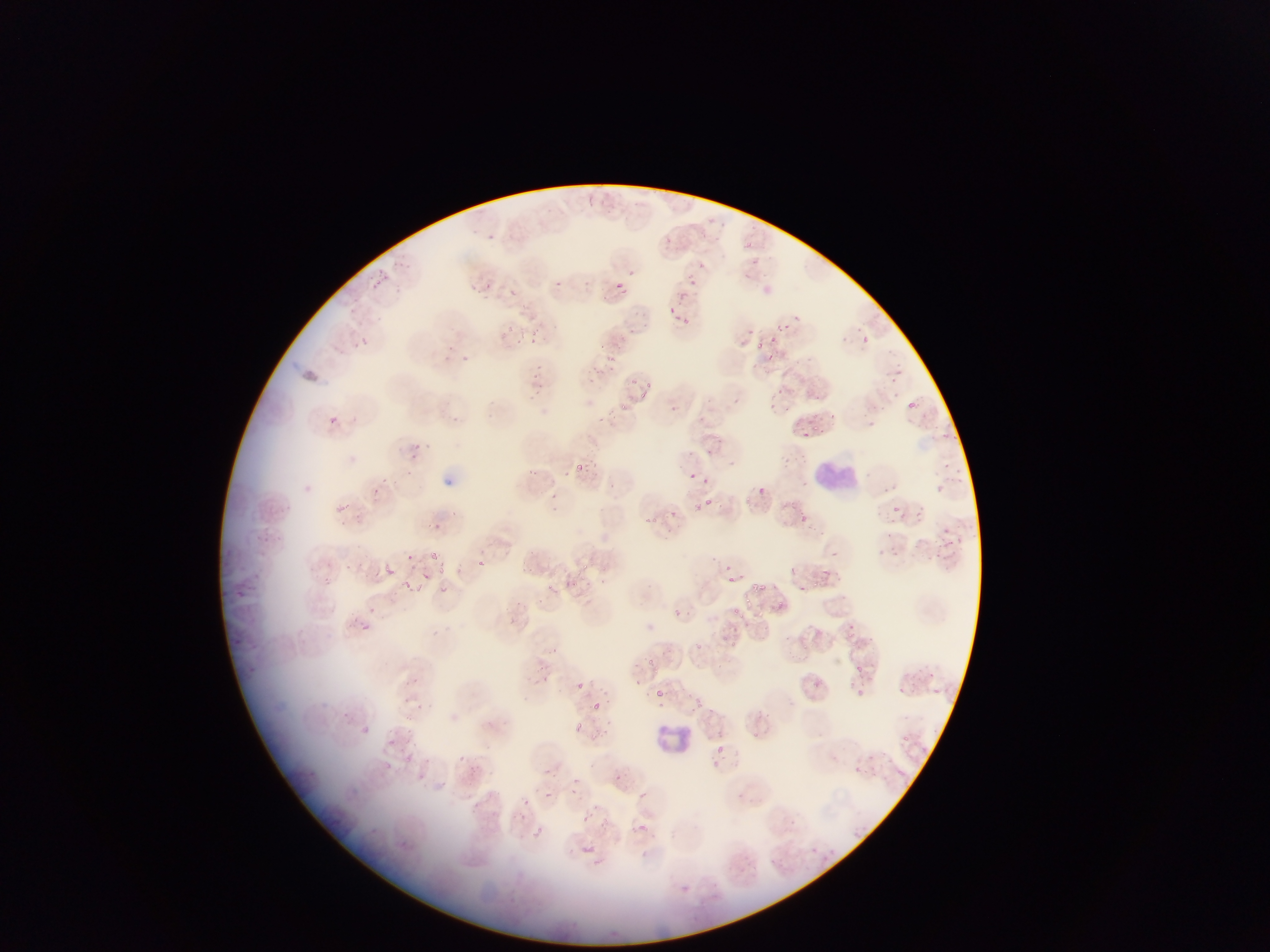

Approximate bounding boxes as [left, top, right, bottom] in pixels. Leukocyte locations: [810, 455, 858, 498], [652, 716, 700, 759]. Plasmodium parasite locations: [471, 230, 485, 239], [488, 233, 499, 244], [714, 234, 721, 244], [665, 235, 674, 248], [746, 241, 754, 248], [698, 261, 709, 274], [628, 268, 634, 276], [371, 273, 388, 287], [685, 275, 698, 287], [556, 280, 566, 288], [612, 280, 628, 296], [467, 283, 481, 292], [483, 283, 496, 294], [508, 288, 519, 297], [678, 290, 690, 301], [669, 306, 674, 314], [682, 315, 690, 324], [777, 315, 799, 334], [502, 318, 524, 346], [642, 322, 648, 331], [849, 322, 872, 348], [532, 327, 541, 337], [521, 329, 527, 339], [357, 334, 371, 348], [767, 335, 775, 344], [755, 339, 762, 350], [444, 342, 454, 349], [460, 354, 470, 363], [605, 354, 614, 362], [593, 366, 603, 372], [585, 371, 597, 381], [532, 372, 540, 379], [630, 379, 640, 384], [645, 379, 657, 388], [637, 387, 651, 400], [533, 388, 544, 397], [906, 392, 924, 411], [617, 401, 627, 410], [668, 404, 679, 413], [607, 407, 618, 416], [328, 414, 340, 426], [599, 416, 615, 425], [797, 421, 811, 446], [812, 424, 818, 432], [410, 442, 420, 451], [574, 463, 587, 474], [690, 471, 701, 482], [758, 484, 767, 496], [744, 494, 753, 503], [705, 498, 713, 504], [891, 505, 901, 513], [798, 512, 809, 523], [646, 514, 658, 523], [406, 548, 423, 565], [428, 551, 438, 560], [478, 559, 487, 568], [581, 562, 592, 572], [381, 566, 400, 579], [438, 568, 448, 578], [424, 573, 437, 583], [728, 575, 736, 584], [580, 577, 589, 581], [573, 580, 584, 589], [811, 581, 818, 589], [400, 582, 410, 591], [546, 582, 559, 594], [753, 583, 767, 591], [797, 584, 811, 592], [744, 595, 755, 606], [676, 607, 686, 618], [734, 607, 748, 617], [363, 623, 374, 638], [691, 640, 702, 650], [538, 644, 561, 662], [645, 658, 658, 666], [857, 665, 864, 674], [410, 673, 421, 685], [657, 690, 665, 697], [403, 694, 416, 703], [593, 700, 606, 709], [574, 719, 587, 732], [405, 723, 416, 737], [751, 731, 762, 742], [712, 746, 730, 758], [405, 756, 410, 766], [571, 778, 579, 786], [542, 790, 552, 798], [638, 792, 647, 800], [582, 814, 592, 824] | approximate [x, y] pixel centers of objects too small to bound: [677, 318], [631, 331], [600, 347], [538, 365], [543, 384], [606, 568], [780, 604], [582, 684]. Collected in Ghana. Mobile-phone photograph taken through the microscope. Thin blood film. Image is 1270×952 pixels. One field of view.